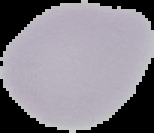

Summary:
  - Image size: 154×133 pixels
  - Result: no Plasmodium parasites seen
  - Preparation: thin blood film
  - Image type: cell region segmented out of the field of view; surrounding area masked to black